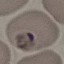

Summary:
  - Malaria status: uninfected
  - Image type: automatically extracted cell patch, resized to 64 × 64 pixels
  - Preparation: thin smear
  - Capture: smartphone camera at the microscope eyepiece
  - Stain: Giemsa